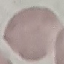
{
  "malaria_status": "uninfected",
  "stain": "Giemsa",
  "preparation": "thin blood smear",
  "capture": "smartphone camera at the microscope eyepiece",
  "image_type": "cell patch, automatically extracted from a larger field of view and resized to 64 × 64 pixels"
}